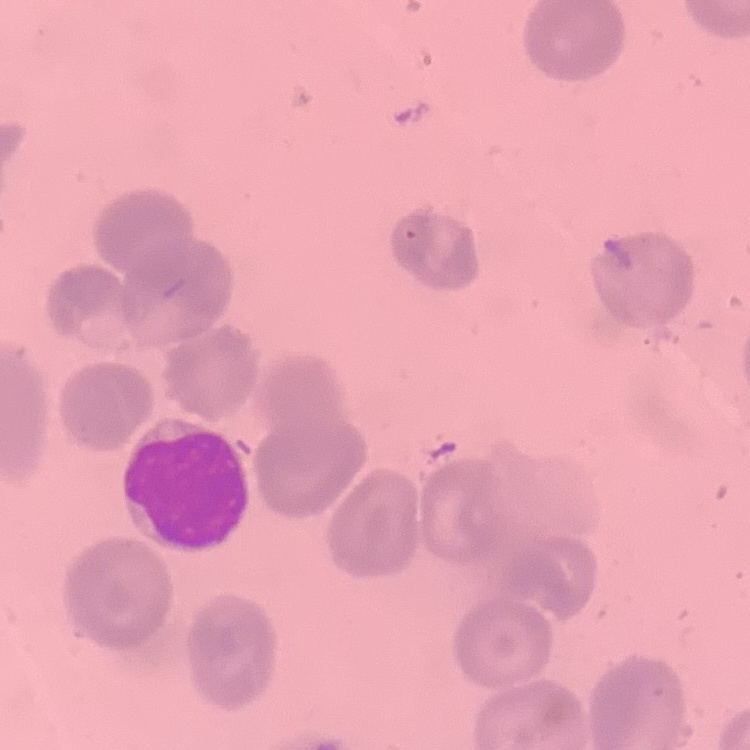

erythrocyte morphology = no rouleaux formation
stain = Field's or Giemsa
image type = one tile cut from a larger photomicrograph
preparation = thin peripheral smear